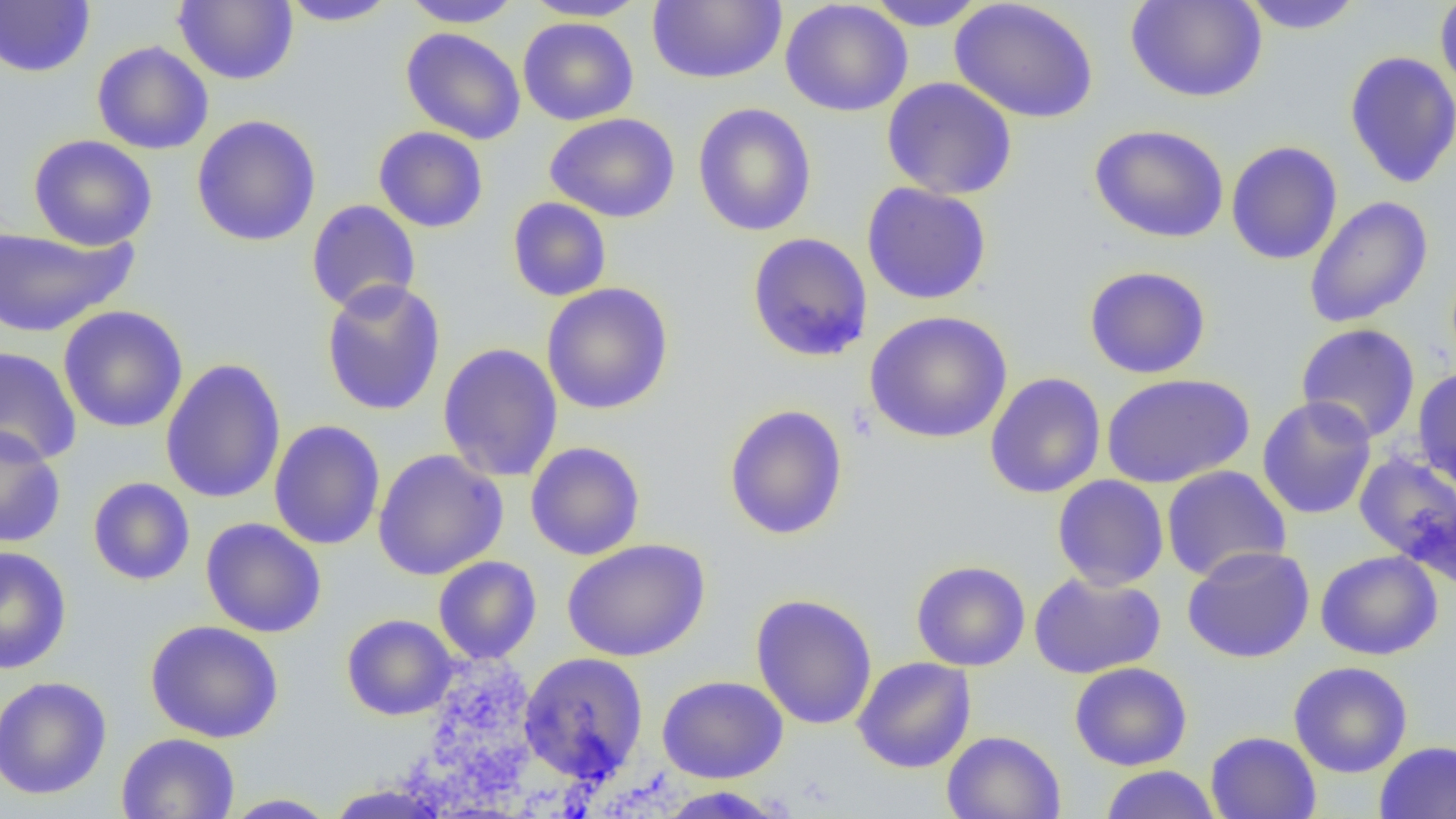
{
  "slide_level_diagnosis": "no evidence of blood parasites",
  "uninfected_red_blood_cell_locations": "approximate bounding boxes as (x1,y1)-(x2,y2) corner pairs in pixels: (174,0)-(298,86), (278,0)-(401,27), (399,0)-(525,28), (521,0)-(650,22), (780,0)-(913,117), (862,0)-(990,31), (949,0)-(1101,124), (1125,0)-(1267,103), (1237,0)-(1365,34), (1435,0)-(1456,101), (0,1)-(95,78), (647,1)-(787,84), (517,17)-(639,126), (400,27)-(526,144), (92,41)-(214,155), (1343,51)-(1456,189), (881,76)-(1018,200), (692,102)-(817,237), (544,112)-(681,223), (191,114)-(322,247), (1089,124)-(1229,244), (373,127)-(489,233), (28,134)-(157,250), (1225,140)-(1343,265), (861,182)-(992,305), (1303,196)-(1433,328), (507,197)-(612,302), (306,199)-(421,315), (0,224)-(136,337), (746,232)-(873,362), (1084,265)-(1211,379), (320,279)-(447,417), (541,282)-(674,415), (58,305)-(188,433), (864,310)-(1013,444), (1295,323)-(1421,444), (438,342)-(563,482), (0,346)-(82,466), (159,357)-(286,504), (1412,366)-(1456,492), (984,372)-(1106,499), (1102,373)-(1254,488), (1257,396)-(1377,520), (723,404)-(849,541), (269,420)-(386,551), (0,427)-(66,548), (525,441)-(645,560), (372,449)-(508,580), (1353,453)-(1456,580), (1161,465)-(1291,581), (1052,474)-(1169,590), (87,477)-(195,586), (201,517)-(327,638), (561,539)-(711,662), (1182,544)-(1316,663), (0,545)-(72,675), (1315,550)-(1444,660), (433,556)-(542,664), (911,559)-(1030,671), (1029,571)-(1166,679), (750,594)-(878,730), (341,614)-(458,720), (145,619)-(284,743), (519,651)-(649,783), (852,656)-(976,773), (1069,661)-(1192,771), (1288,661)-(1413,778), (0,675)-(112,800), (657,675)-(789,783), (941,730)-(1066,819), (1206,731)-(1321,819), (115,733)-(240,819), (1374,740)-(1456,819), (1100,765)-(1221,818), (652,786)-(792,818), (220,793)-(339,818)",
  "modality": "light microscopy",
  "magnification": "1000x",
  "image_size": "1456×819 pixels",
  "field_of_view": "single",
  "preparation": "thin blood smear"
}